Locate and identify every blood parasite.
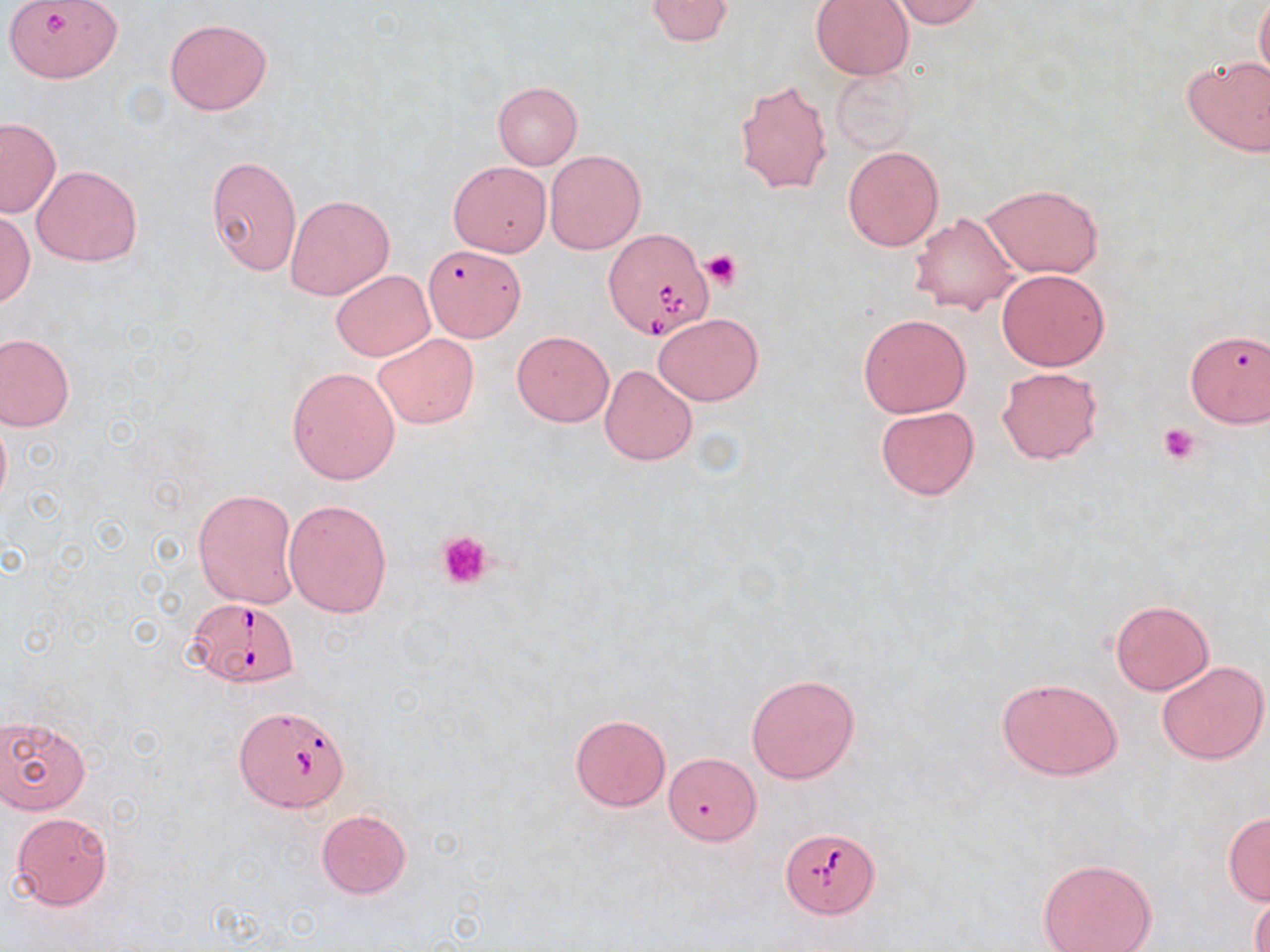
Approximate bounding boxes as [x1, y1, x2, y2] in pixels.
Babesia divergens-infected red blood cells: [604, 227, 714, 339], [185, 597, 300, 688], [236, 706, 351, 811], [780, 827, 879, 918].
No Plasmodium falciparum, Plasmodium ovale, Plasmodium malariae, Plasmodium vivax, or Trypanosoma brucei observed.

Uninfected red blood cell locations: [6, 0, 136, 87], [645, 0, 735, 46], [810, 0, 914, 80], [892, 0, 985, 28], [1256, 0, 1270, 90], [165, 16, 273, 116], [1180, 53, 1270, 158], [828, 64, 918, 154], [735, 80, 832, 194], [492, 81, 583, 169], [0, 117, 61, 219], [842, 145, 944, 251], [544, 150, 645, 254], [205, 154, 303, 276], [450, 160, 552, 256], [31, 164, 142, 267], [981, 183, 1104, 278], [285, 195, 395, 301], [1, 210, 34, 308], [911, 212, 1020, 316], [422, 245, 526, 346], [996, 269, 1109, 371], [331, 270, 434, 360], [653, 312, 762, 406], [858, 313, 972, 417], [1185, 329, 1270, 427], [512, 331, 614, 426], [1, 333, 75, 430], [374, 333, 478, 428], [599, 364, 697, 465], [997, 366, 1102, 463], [286, 367, 400, 484], [875, 404, 980, 501], [0, 411, 11, 513], [192, 489, 299, 609], [284, 499, 393, 618], [1109, 599, 1214, 695], [1156, 659, 1269, 763], [745, 673, 860, 784], [996, 677, 1123, 781], [570, 713, 670, 810], [1, 715, 91, 813], [664, 752, 760, 845], [316, 809, 412, 898], [1223, 811, 1270, 905], [10, 813, 112, 909], [1038, 857, 1157, 952], [1249, 887, 1270, 952]. Platelet locations: [703, 250, 739, 289], [1158, 422, 1200, 464], [435, 531, 495, 590]. Slide-level diagnosis: Babesia divergens. Image is 1270×952 pixels. Captured at 1000x magnification. Thin blood film. May-Grünwald-Giemsa-stained preparation. Light microscopy. Single field of view.